Give a bounding box for every leukocyte visible.
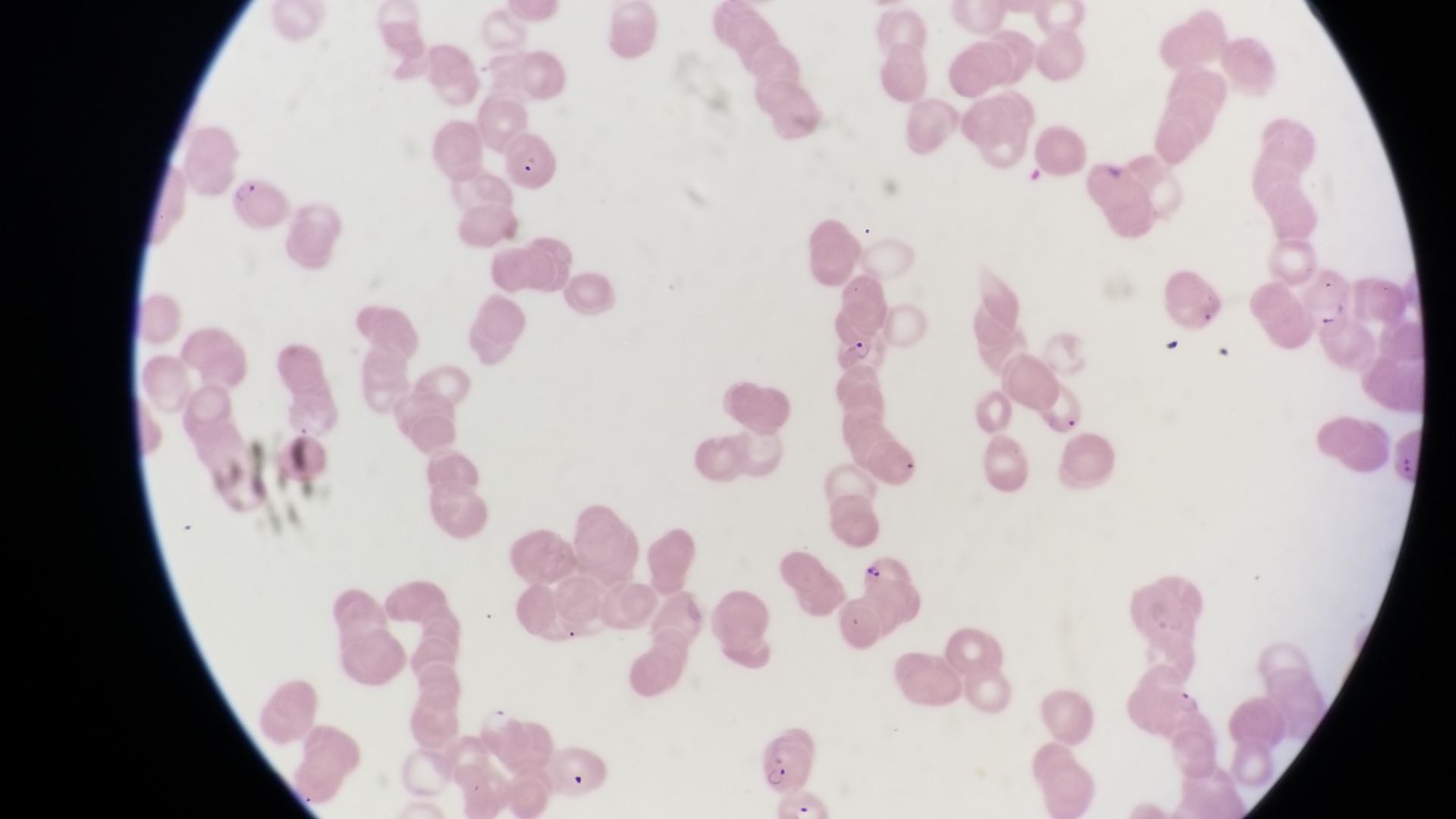
No leukocytes observed.

Approximate bounding boxes as [left, top, right, bottom] in pixels.
Summary:
  - Parasitised red blood cell locations: [497, 132, 558, 201], [228, 178, 288, 233], [1308, 288, 1361, 337], [836, 330, 885, 372], [852, 552, 919, 608], [758, 736, 825, 796]
  - Capture: smartphone photograph through the eyepiece of an Olympus CX-23 microscope
  - Magnification: 1000x
  - Country: Uganda
  - Field of view: single
  - Image size: 1456×819 pixels
  - Preparation: thin blood smear